Classify this cell by malaria status.
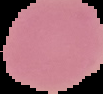

It is uninfected.

image size = 103×94 pixels
preparation = thin blood film
image type = cell region segmented out of the field of view; surrounding area masked to black